Assess the morphology of the erythrocytes.
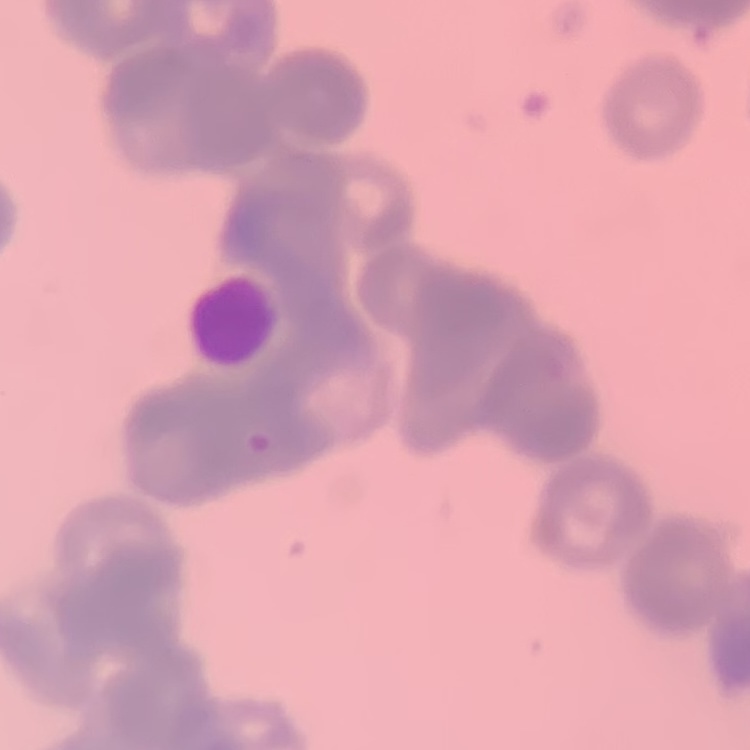

They show rouleaux formation.

image type = one tile cut from a larger photomicrograph
preparation = thin blood film
stain = Field's or Giemsa